Assess the morphology of the erythrocytes.
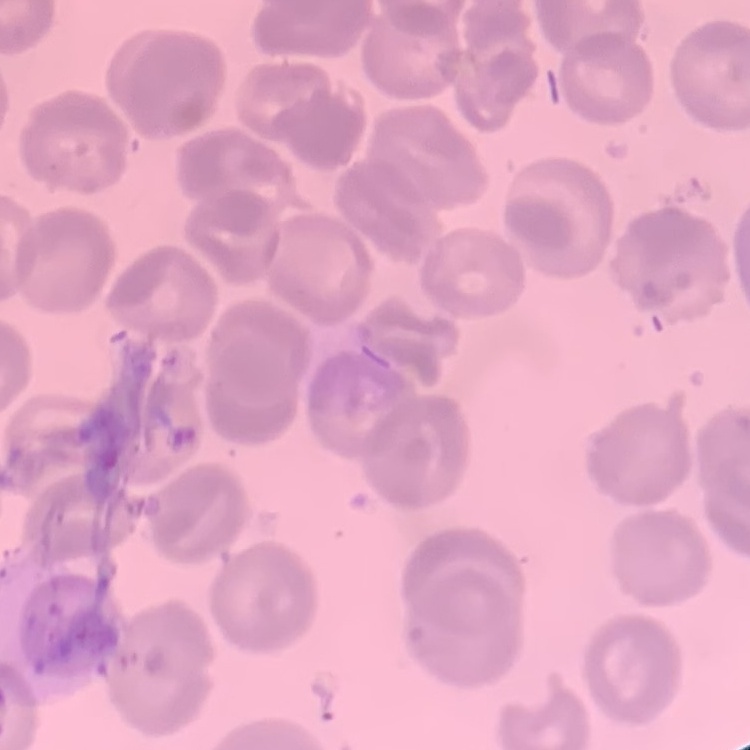

No rouleaux formation.

image type = one tile cut from a larger photomicrograph
stain = Field's or Giemsa
preparation = thin blood smear